Report the malaria status of this cell.
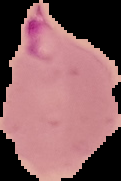
Parasitized.

Summary:
  - Image size: 121×181 pixels
  - Preparation: thin blood smear
  - Image type: segmented cell region with the area outside set to black